Classify this cell by malaria status.
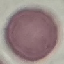

Uninfected.

Giemsa-stained preparation. Thin blood smear. Cell patch, automatically extracted from a larger field of view and resized to 64 × 64 pixels. Acquired by smartphone through the microscope eyepiece.